State which cell type is depicted.
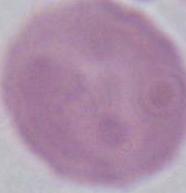

An erythrocyte.

magnification: 1000x
modality: micrograph